Assess this cell for malaria.
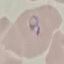

It is parasitized.

capture: smartphone through the microscope eyepiece
stain: Giemsa
preparation: thin blood smear
image_type: automatically extracted cell patch, resized to 64 × 64 pixels